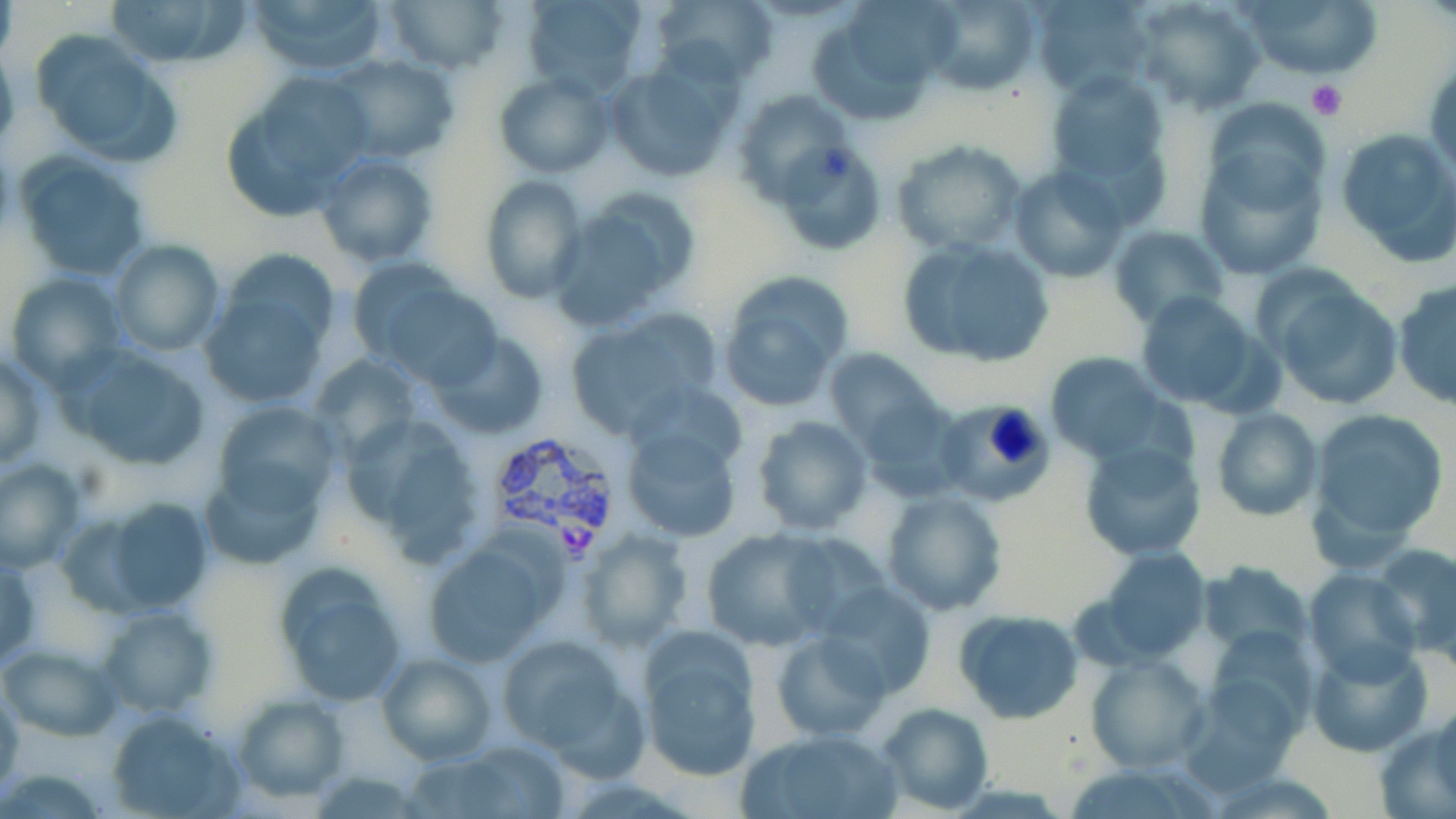 Approximate bounding boxes as named x1/y1/x2/y2 corners in pixels. Platelet locations: (x1=1305, y1=80, x2=1346, y2=119). Uninfected red blood cell locations: (x1=102, y1=0, x2=250, y2=67), (x1=246, y1=0, x2=390, y2=78), (x1=384, y1=0, x2=507, y2=75), (x1=520, y1=0, x2=649, y2=98), (x1=650, y1=0, x2=777, y2=87), (x1=917, y1=0, x2=1040, y2=92), (x1=1031, y1=0, x2=1153, y2=96), (x1=1130, y1=0, x2=1265, y2=113), (x1=1237, y1=0, x2=1381, y2=79), (x1=29, y1=30, x2=179, y2=166), (x1=0, y1=44, x2=19, y2=156), (x1=327, y1=54, x2=458, y2=164), (x1=605, y1=61, x2=740, y2=183), (x1=1038, y1=66, x2=1174, y2=218), (x1=494, y1=71, x2=613, y2=179), (x1=222, y1=74, x2=374, y2=217), (x1=732, y1=87, x2=849, y2=203), (x1=1334, y1=124, x2=1456, y2=266), (x1=892, y1=139, x2=1029, y2=256), (x1=773, y1=141, x2=888, y2=255), (x1=1193, y1=143, x2=1326, y2=282), (x1=315, y1=150, x2=439, y2=269), (x1=14, y1=151, x2=152, y2=281), (x1=1008, y1=165, x2=1129, y2=281), (x1=480, y1=175, x2=588, y2=303), (x1=552, y1=187, x2=699, y2=328), (x1=1107, y1=225, x2=1230, y2=330), (x1=894, y1=235, x2=1057, y2=368), (x1=109, y1=238, x2=225, y2=358), (x1=346, y1=263, x2=499, y2=386), (x1=5, y1=272, x2=127, y2=390), (x1=716, y1=275, x2=850, y2=413), (x1=1262, y1=275, x2=1405, y2=412), (x1=197, y1=277, x2=333, y2=411), (x1=1393, y1=282, x2=1456, y2=411), (x1=1134, y1=290, x2=1271, y2=415), (x1=563, y1=311, x2=719, y2=438), (x1=428, y1=332, x2=553, y2=441), (x1=60, y1=345, x2=213, y2=471), (x1=823, y1=347, x2=938, y2=450), (x1=0, y1=349, x2=49, y2=470), (x1=1043, y1=351, x2=1171, y2=462), (x1=308, y1=352, x2=424, y2=460), (x1=855, y1=394, x2=968, y2=502), (x1=210, y1=400, x2=344, y2=518), (x1=932, y1=401, x2=1053, y2=507), (x1=1211, y1=407, x2=1322, y2=522), (x1=1307, y1=407, x2=1449, y2=553), (x1=338, y1=413, x2=483, y2=558), (x1=751, y1=415, x2=872, y2=534), (x1=619, y1=417, x2=744, y2=545), (x1=1077, y1=440, x2=1205, y2=559), (x1=0, y1=458, x2=86, y2=574), (x1=199, y1=458, x2=329, y2=569), (x1=881, y1=489, x2=1007, y2=614), (x1=87, y1=494, x2=218, y2=616), (x1=700, y1=527, x2=838, y2=652), (x1=576, y1=528, x2=693, y2=652), (x1=419, y1=537, x2=560, y2=668), (x1=1373, y1=543, x2=1456, y2=659), (x1=1095, y1=547, x2=1209, y2=661), (x1=0, y1=548, x2=41, y2=672), (x1=272, y1=562, x2=412, y2=707), (x1=1200, y1=563, x2=1314, y2=651), (x1=1304, y1=567, x2=1420, y2=683), (x1=815, y1=582, x2=937, y2=703), (x1=96, y1=604, x2=218, y2=718), (x1=953, y1=609, x2=1085, y2=723), (x1=1210, y1=626, x2=1315, y2=739), (x1=635, y1=628, x2=763, y2=783), (x1=772, y1=630, x2=891, y2=740), (x1=497, y1=634, x2=642, y2=765), (x1=1308, y1=640, x2=1432, y2=759), (x1=0, y1=642, x2=120, y2=742), (x1=375, y1=652, x2=497, y2=766), (x1=1087, y1=653, x2=1209, y2=772), (x1=0, y1=683, x2=23, y2=791), (x1=232, y1=694, x2=348, y2=803), (x1=877, y1=703, x2=993, y2=814), (x1=104, y1=706, x2=245, y2=817), (x1=1378, y1=706, x2=1456, y2=817), (x1=737, y1=727, x2=905, y2=819), (x1=438, y1=740, x2=573, y2=818), (x1=308, y1=767, x2=429, y2=817). Plasmodium vivax-infected red blood cell locations: (x1=485, y1=430, x2=626, y2=552). Slide-level diagnosis: Plasmodium vivax. One field of a larger specimen. 1000x magnification. Light microscopy. May-Grünwald-Giemsa-stained preparation. Image is 1456×819 pixels. Thin blood smear.